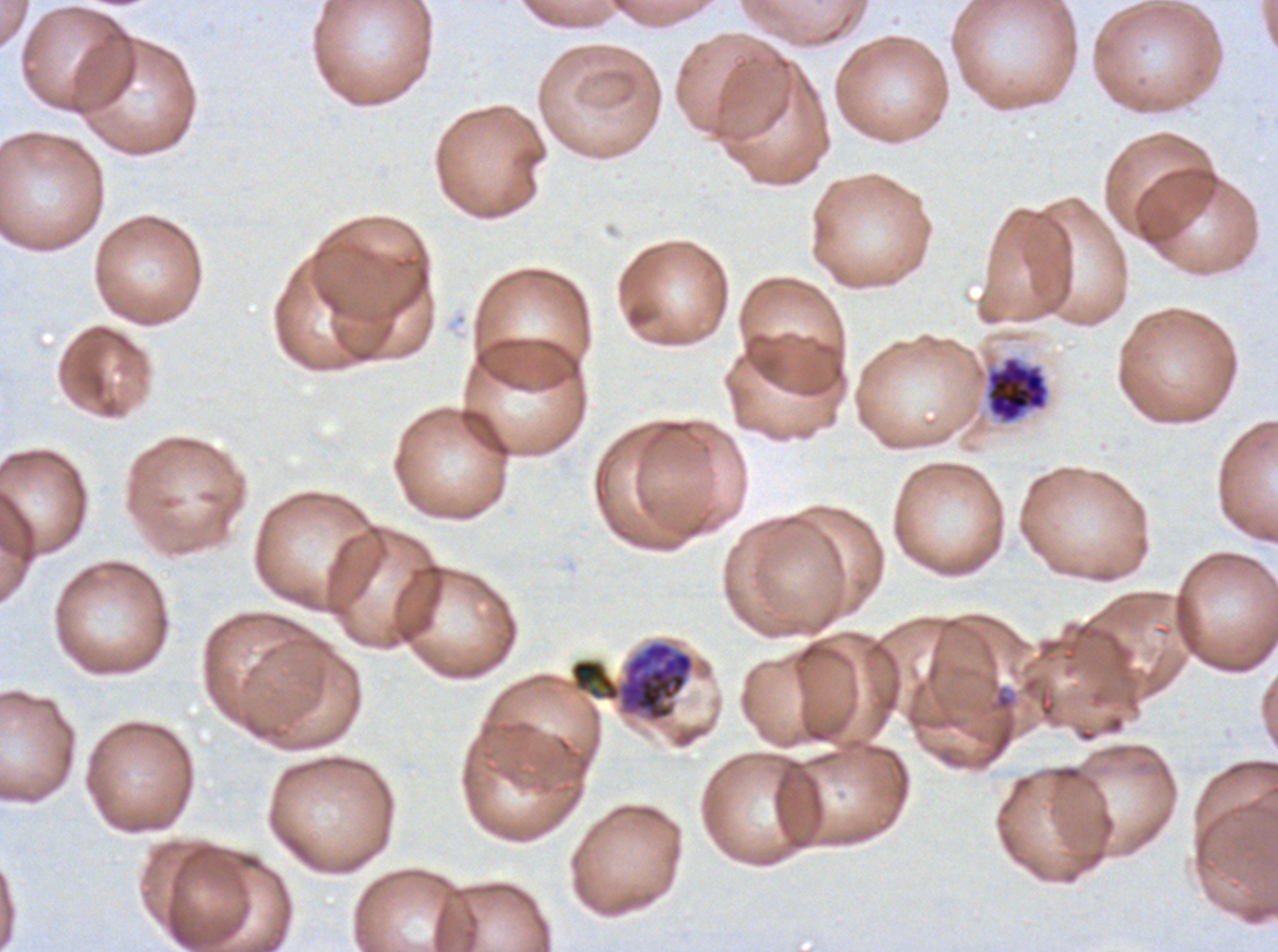
notation = approximate bounding rectangles given as corner coordinates in pixels from the top-left
early schizont locations = (x1=570, y1=641, x2=694, y2=722)
late schizont locations = (x1=987, y1=357, x2=1049, y2=422)
life-cycle stages observed = early schizont, late schizont
preparation = thin blood smear
image size = 1278×952 pixels
specimen = P. falciparum from a patient in The Gambia, cultured ex vivo for 24 to 48 hours
stain = Giemsa
field of view = one sub-image of a larger composite